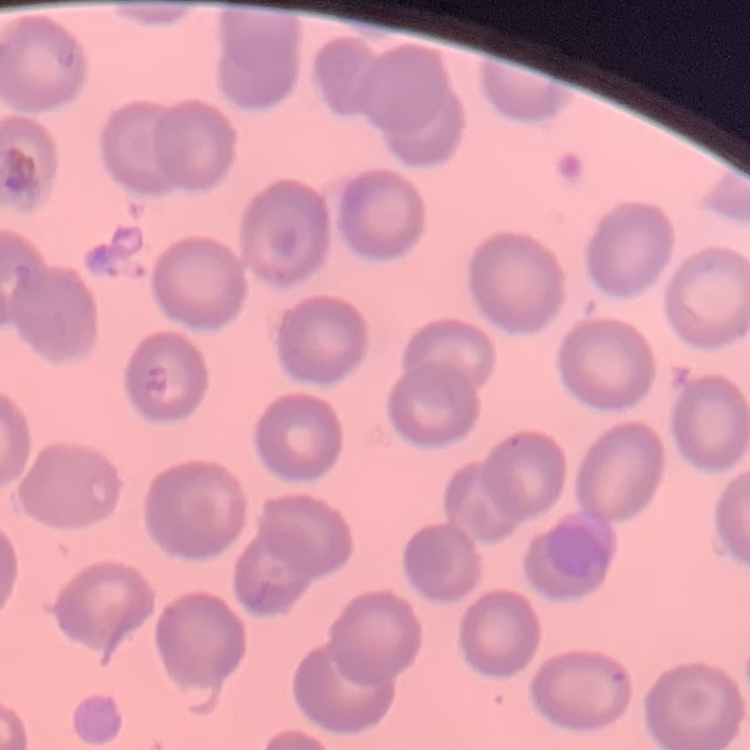
Summary:
  - Erythrocyte morphology: no rouleaux formation
  - Image type: square crop of a larger photomicrograph
  - Preparation: thin blood film
  - Stain: Field's or Giemsa